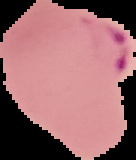
image_size: 136×160 pixels
preparation: thin blood film
malaria_status: parasitized
image_type: cell region segmented out of the field of view; surrounding area masked to black